Evaluate for malaria.
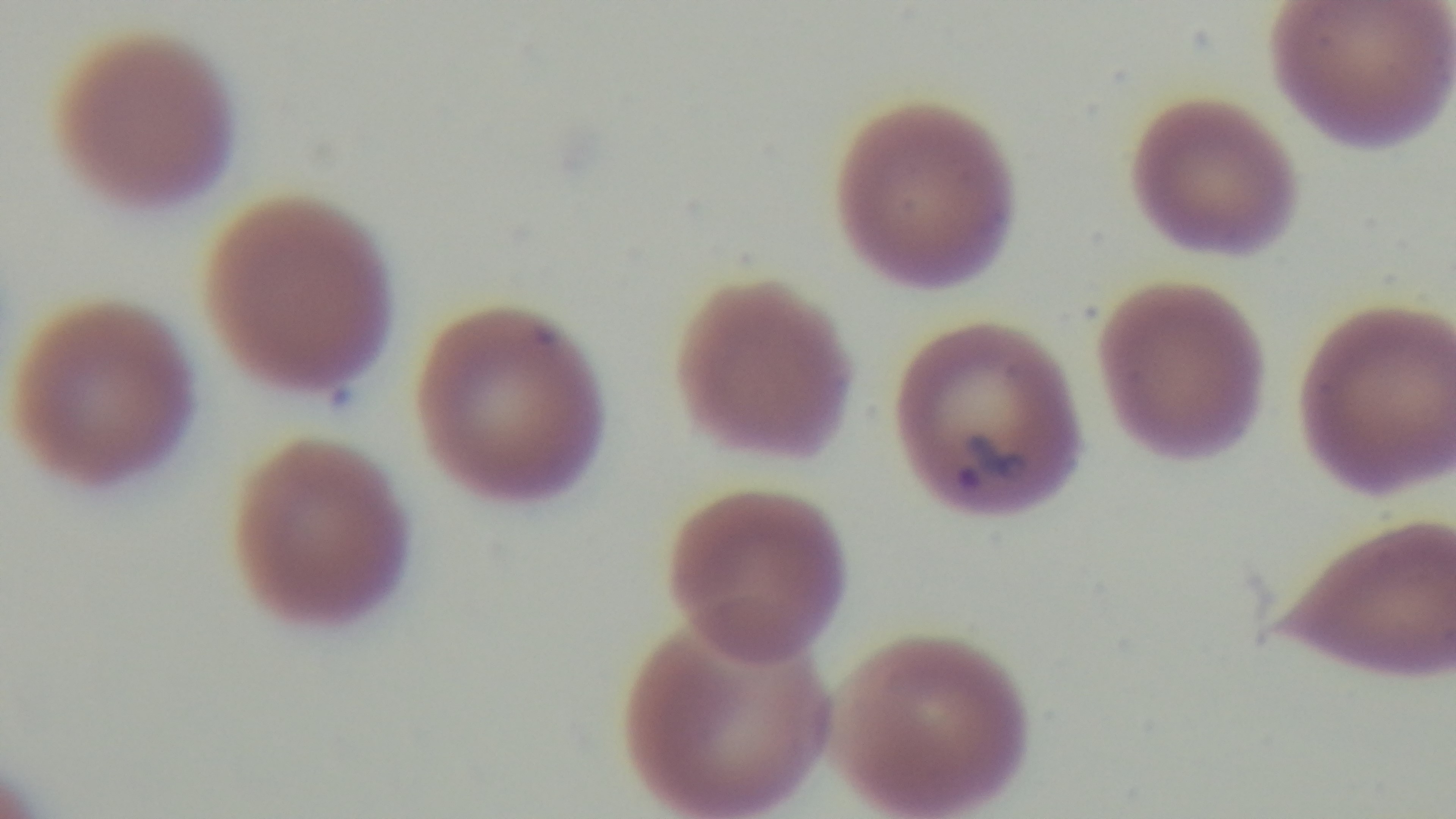

Infected.

Summary:
  - Field of view: single
  - Objective: 100x oil immersion
  - Stain: Giemsa
  - Capture: mounted 4K digital camera
  - Modality: light microscopy
  - Preparation: thin blood film